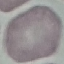
Malaria status: uninfected. Cell patch, automatically extracted from a larger field of view and resized to 64 × 64 pixels. Giemsa-stained preparation. Photographed with a smartphone camera at the microscope eyepiece. Thin blood film.